State which cell type is depicted.
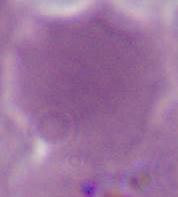

This is an erythrocyte.

modality = micrograph
magnification = 1000x